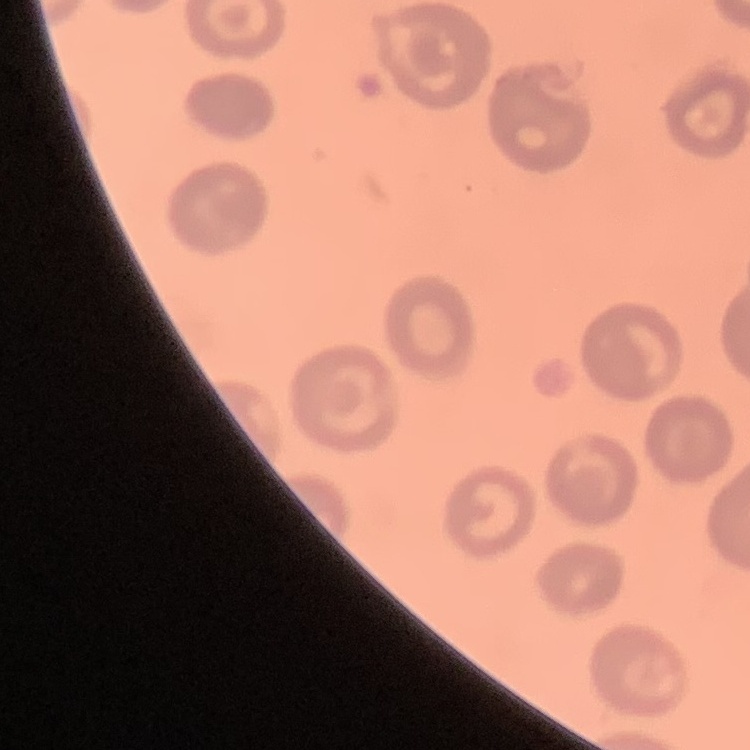
Summary:
  - Erythrocyte morphology: no rouleaux formation
  - Stain: Field's or Giemsa
  - Preparation: thin blood film
  - Image type: square crop of a larger photomicrograph